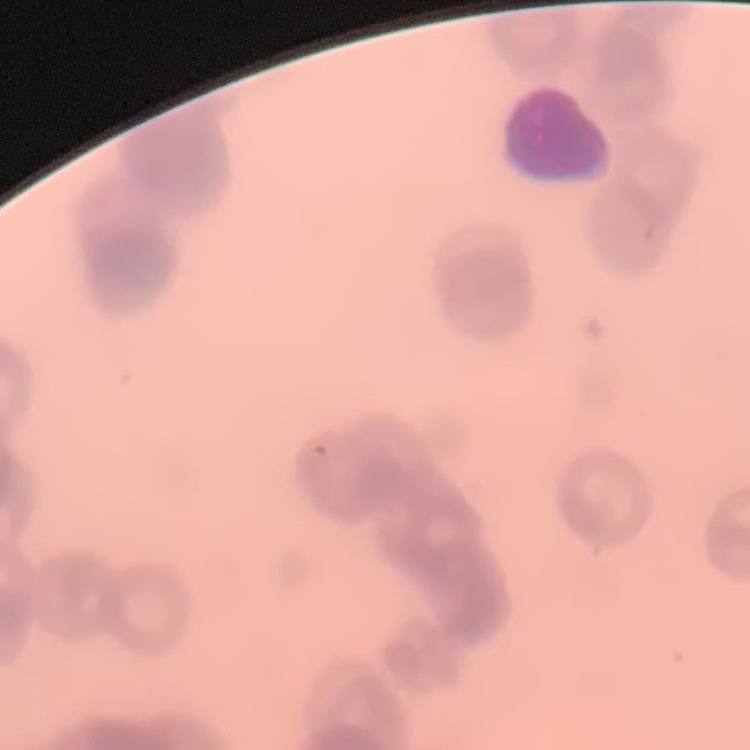
erythrocyte morphology = rouleaux formation
stain = Field's or Giemsa
preparation = thin peripheral smear
image type = square crop of a larger photomicrograph